Report the malaria status of this cell.
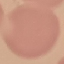

Uninfected.

{
  "capture": "smartphone through the microscope eyepiece",
  "image_type": "cell patch, automatically extracted from a larger field of view and resized to 64 × 64 pixels",
  "preparation": "thin smear",
  "stain": "Giemsa"
}